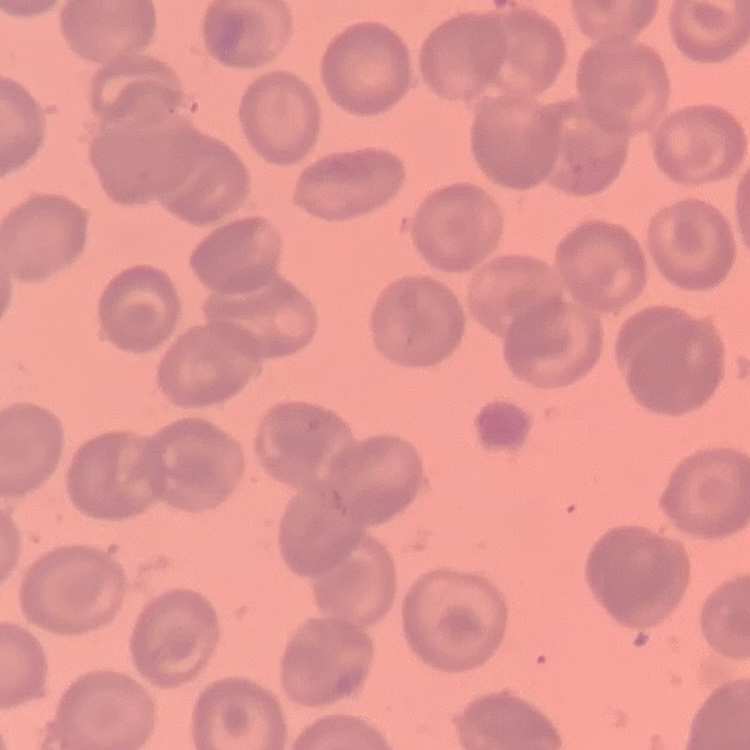
{
  "red_blood_cell_morphology": "no rouleaux formation",
  "stain": "Field's or Giemsa",
  "preparation": "thin blood film",
  "image_type": "one tile cut from a larger photomicrograph"
}